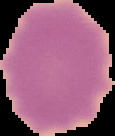

image type = segmented cell region on a black background
image size = 115×136 pixels
preparation = thin blood smear
result = negative for Plasmodium parasites